Identify the parasite.
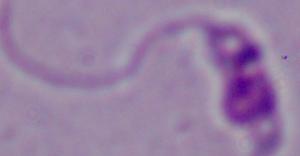
Leishmania.

Summary:
  - Magnification: 1000x
  - Modality: micrograph